Identify the parasite.
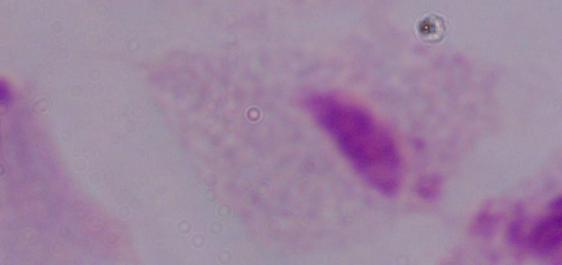
A trichomonad.

1000x magnification. Photomicrograph.